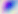

Toxoplasma gondii is shown. Micrograph. Captured at 400x magnification.